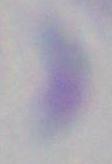
Summary:
  - Modality: photomicrograph
  - Identification: Toxoplasma gondii
  - Magnification: 1000x